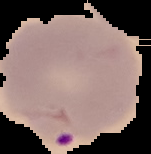

Image is 151×154 pixels. Malaria status: parasitized. From a thin blood smear. Segmented cell region on a black background.